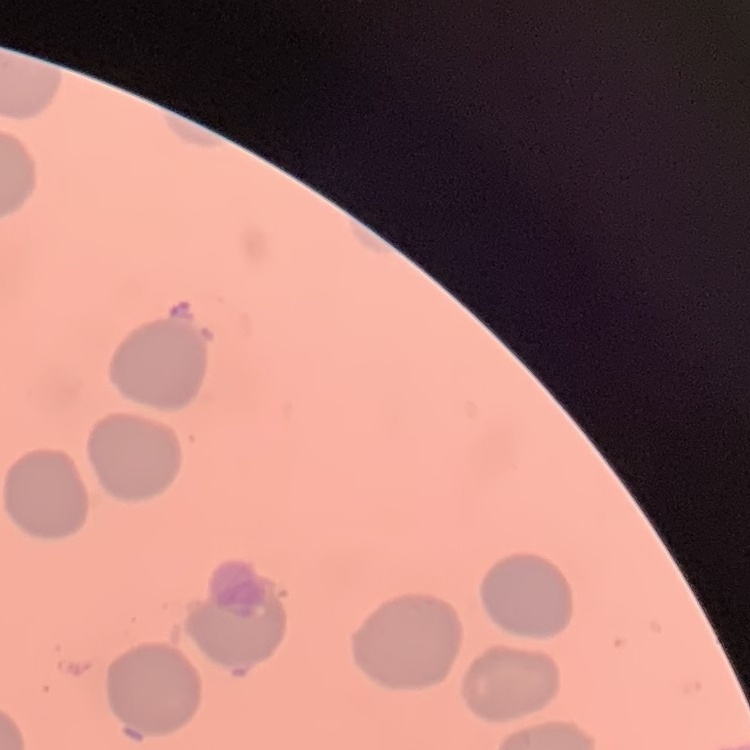
red blood cell morphology = no rouleaux formation
image type = one tile cut from a larger photomicrograph
stain = Field's or Giemsa
preparation = thin blood smear